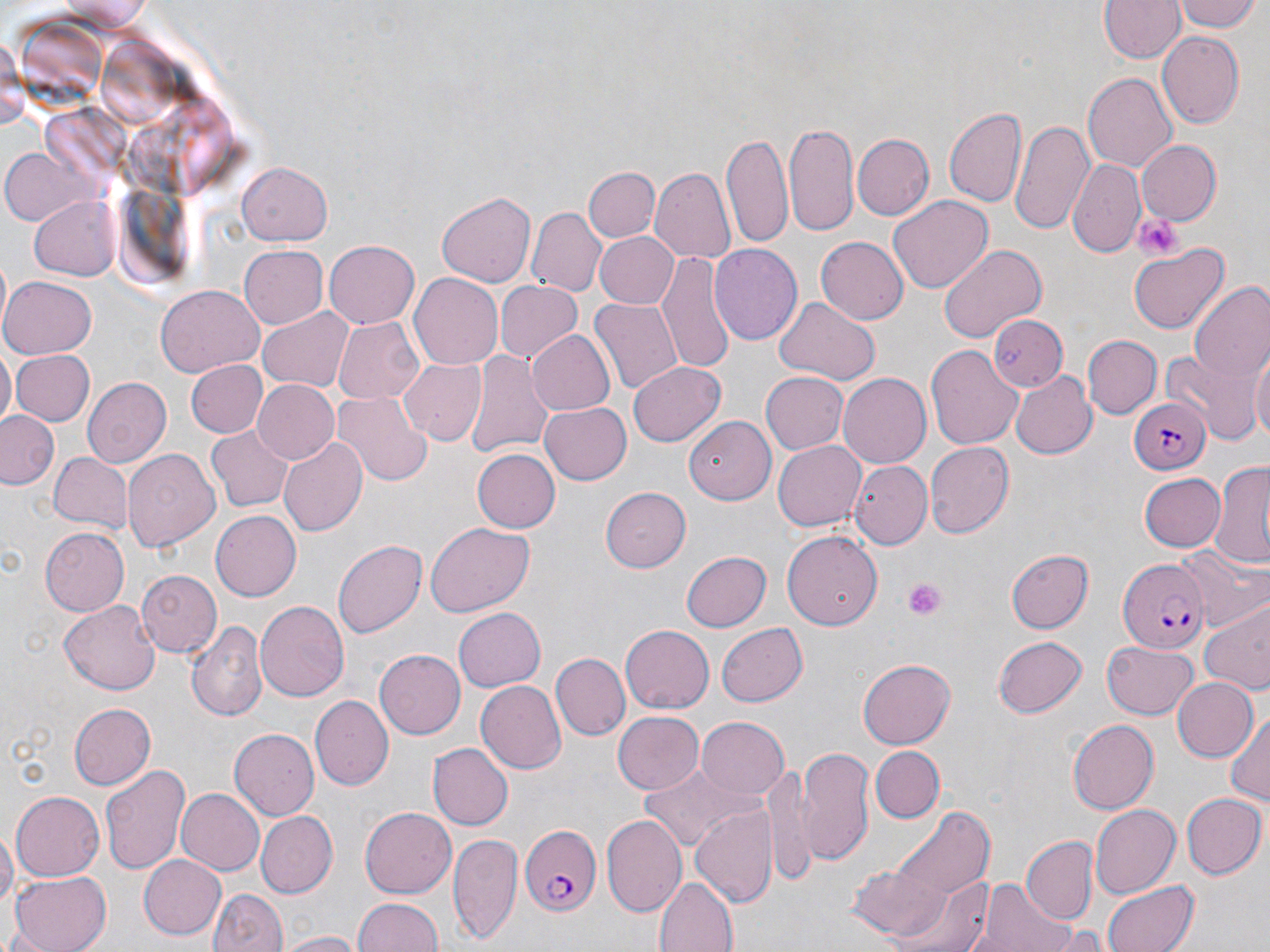 Approximate bounding boxes as (x1, y1, x2, y2) in pixels. Plasmodium falciparum-infected red blood cell locations: (1126, 397, 1211, 473), (1118, 559, 1210, 652), (518, 824, 604, 916). Platelet locations: (1135, 212, 1183, 261), (903, 577, 947, 620). Uninfected red blood cell locations: (1097, 0, 1186, 65), (1174, 0, 1263, 32), (2, 29, 27, 135), (1155, 30, 1243, 127), (1084, 72, 1177, 172), (944, 103, 1025, 207), (1010, 119, 1091, 235), (784, 122, 859, 238), (721, 132, 794, 250), (853, 133, 933, 218), (1136, 139, 1222, 226), (2, 144, 93, 226), (1068, 157, 1146, 255), (236, 161, 333, 244), (585, 166, 659, 243), (650, 169, 734, 264), (437, 191, 536, 285), (28, 194, 120, 282), (889, 194, 993, 294), (526, 207, 605, 297), (596, 231, 678, 310), (816, 236, 908, 325), (325, 238, 420, 328), (1126, 242, 1231, 333), (240, 244, 328, 327), (708, 245, 802, 346), (937, 245, 1045, 344), (657, 249, 736, 377), (407, 272, 503, 369), (1, 277, 98, 359), (495, 281, 581, 363), (1189, 283, 1270, 383), (156, 287, 262, 374), (591, 295, 683, 398), (773, 296, 880, 384), (258, 302, 355, 392), (987, 314, 1066, 393), (332, 316, 425, 404), (524, 327, 616, 417), (1083, 334, 1161, 419), (927, 343, 1023, 447), (1249, 344, 1270, 444), (0, 346, 15, 429), (11, 350, 95, 425), (465, 352, 554, 460), (1166, 352, 1255, 434), (398, 357, 487, 444), (185, 359, 268, 439), (629, 360, 726, 446), (1011, 371, 1097, 458), (758, 372, 846, 455), (837, 373, 932, 468), (80, 376, 171, 467), (251, 379, 339, 463), (333, 390, 430, 486), (538, 401, 631, 485), (0, 411, 61, 489), (685, 414, 775, 505), (205, 426, 293, 511), (279, 436, 368, 538), (771, 439, 866, 532), (925, 443, 1013, 535), (470, 449, 559, 534), (123, 450, 220, 552), (47, 451, 129, 530), (849, 461, 932, 548), (1209, 462, 1270, 567), (1138, 471, 1226, 552), (600, 488, 691, 572), (212, 511, 301, 600), (426, 522, 534, 616), (40, 527, 129, 616), (782, 531, 883, 628), (333, 540, 427, 639), (1179, 544, 1267, 630), (1005, 549, 1093, 634), (682, 550, 770, 631), (136, 570, 222, 656), (60, 600, 161, 695), (254, 600, 351, 701), (1200, 602, 1270, 694), (453, 605, 546, 688), (187, 620, 265, 721), (714, 622, 808, 707), (619, 624, 712, 715), (992, 634, 1087, 719), (1103, 639, 1198, 718), (373, 649, 465, 740), (552, 653, 630, 741), (858, 659, 956, 747), (1171, 677, 1258, 762), (474, 680, 564, 775), (312, 696, 392, 789), (68, 703, 157, 790), (1225, 709, 1270, 808), (612, 710, 705, 793), (695, 718, 790, 799), (1068, 719, 1159, 813), (230, 729, 319, 822), (427, 741, 512, 831), (796, 746, 877, 868), (871, 746, 943, 823), (99, 761, 190, 874), (637, 764, 764, 851), (760, 767, 816, 884), (174, 787, 265, 877), (9, 792, 104, 882), (1181, 793, 1265, 879), (689, 803, 779, 908), (1089, 803, 1180, 900), (358, 806, 457, 899), (890, 807, 994, 906), (254, 811, 336, 898), (602, 814, 687, 920), (1, 827, 15, 916), (449, 833, 521, 945), (1021, 837, 1096, 924), (136, 854, 227, 940), (9, 870, 111, 952), (884, 872, 997, 952), (654, 874, 736, 952), (1101, 879, 1196, 952), (972, 880, 1086, 952), (210, 887, 287, 952), (352, 897, 443, 952), (276, 930, 366, 951). Slide-level diagnosis: Plasmodium falciparum. Image is 1270×952 pixels. 1000x magnification. Thin blood film. Single field of view. Light microscopy. May-Grünwald-Giemsa-stained preparation.